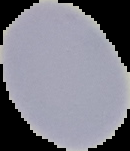
Summary:
  - Result: negative for malaria parasites
  - Image type: cell region segmented out of the field of view; surrounding area masked to black
  - Image size: 130×151 pixels
  - Preparation: thin blood smear